Name the blood parasite species.
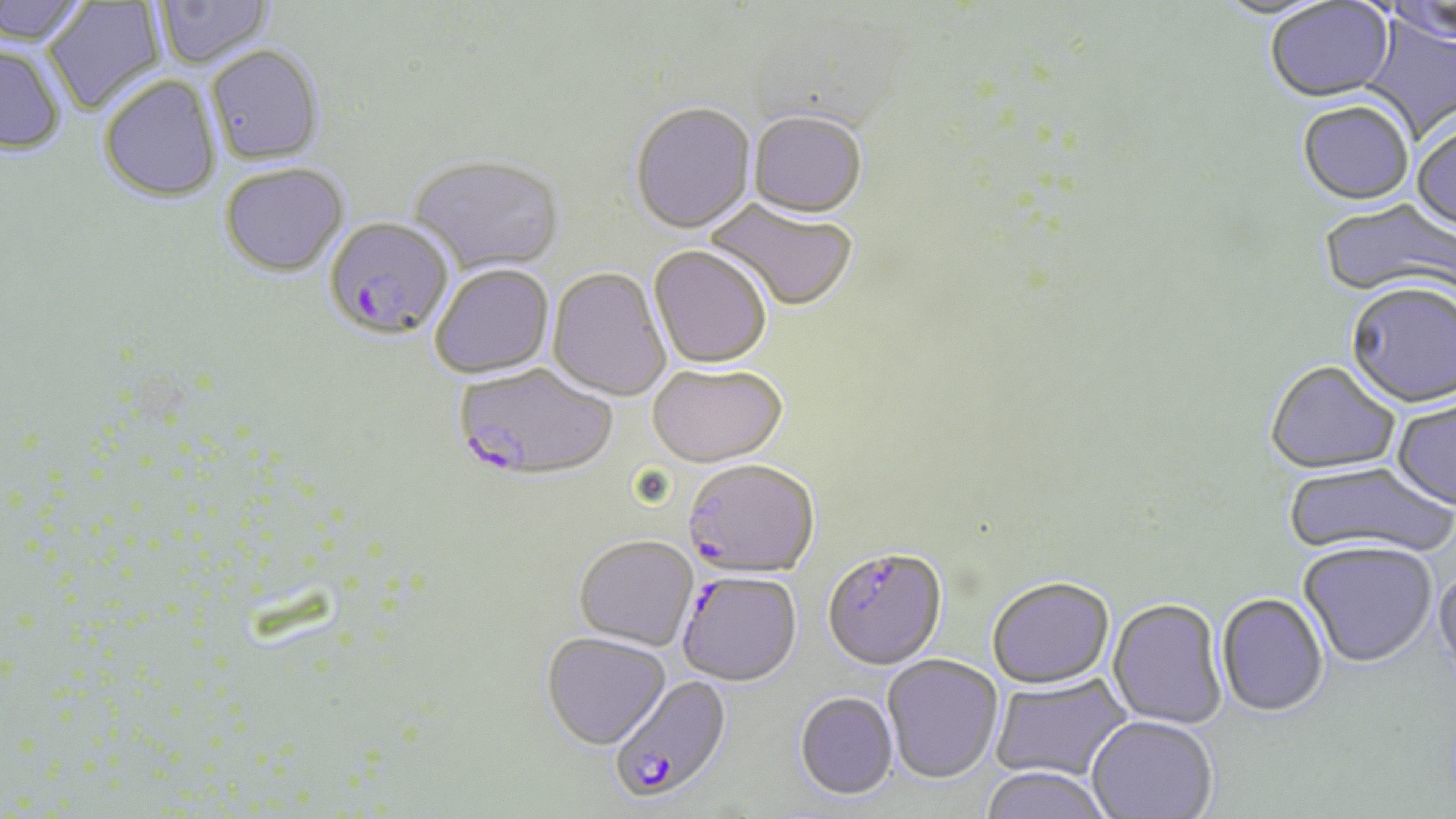
Plasmodium falciparum.

preparation: thin blood film
plasmodium_falciparum_infected_red_blood_cell_locations: 'approximate bounding boxes as (x1, y1, x2, y2) in pixels: (323, 218, 455, 343), (454, 365, 618, 482), (682, 460, 819, 580), (822, 548, 947, 672), (676, 572, 802, 688), (611, 678, 728, 804)'
magnification: 1000x
stain: May-Grünwald-Giemsa
modality: optical microscopy
image_size: 1456×819 pixels
field_of_view: one of a larger specimen
uninfected_red_blood_cell_locations: 'approximate bounding boxes as (x1, y1, x2, y2) in pixels: (0, 0, 92, 48), (42, 0, 167, 116), (153, 0, 273, 70), (1384, 0, 1456, 49), (1264, 1, 1397, 106), (1356, 15, 1456, 143), (0, 45, 66, 155), (205, 47, 325, 168), (98, 77, 222, 204), (630, 104, 756, 237), (1297, 104, 1414, 208), (748, 114, 867, 222), (1411, 123, 1456, 236), (408, 157, 565, 279), (220, 165, 350, 280), (704, 199, 858, 314), (1318, 200, 1455, 302), (648, 247, 771, 371), (430, 266, 554, 380), (546, 269, 671, 403), (1344, 285, 1455, 411), (1265, 362, 1401, 478), (647, 366, 788, 470), (1392, 398, 1456, 513), (1282, 462, 1456, 562), (574, 536, 698, 652), (1298, 543, 1438, 670), (1432, 565, 1456, 684), (986, 578, 1115, 690), (1216, 594, 1329, 718), (1108, 598, 1227, 730), (541, 632, 671, 750), (882, 654, 1004, 784), (990, 673, 1132, 782), (794, 692, 899, 800), (1086, 716, 1217, 818), (980, 766, 1115, 819)'